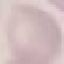

malaria status = uninfected
stain = Giemsa
preparation = thin blood film
capture = smartphone camera at the microscope eyepiece
image type = automatically extracted cell patch, resized to 64 × 64 pixels